Locate platelets.
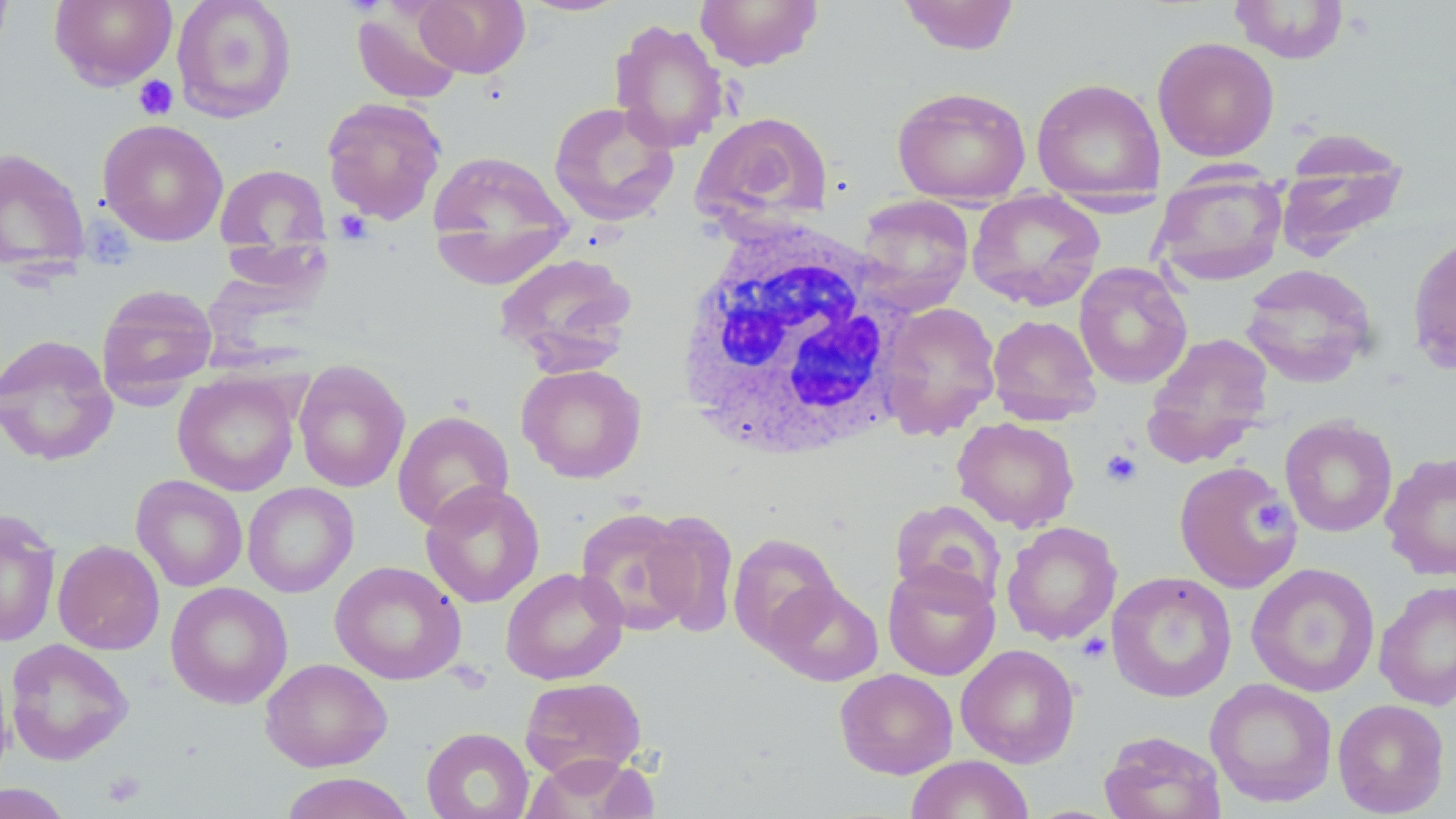
Approximate bounding boxes as (x1, y1, x2, y2) in pixels.
Platelets: (133, 75, 178, 120), (335, 210, 373, 242), (1100, 449, 1143, 488), (1250, 497, 1294, 537), (1077, 633, 1112, 663), (101, 769, 145, 808).

Uninfected red blood cell locations: (0, 0, 14, 65), (49, 0, 178, 89), (171, 0, 297, 123), (413, 0, 531, 78), (517, 0, 630, 17), (694, 0, 824, 71), (897, 0, 1020, 55), (1229, 0, 1350, 64), (351, 3, 466, 106), (609, 18, 730, 153), (1152, 36, 1280, 161), (1031, 78, 1165, 199), (891, 86, 1031, 205), (321, 96, 447, 224), (548, 101, 680, 227), (691, 111, 834, 230), (97, 119, 229, 246), (1276, 133, 1408, 260), (0, 147, 90, 276), (426, 148, 574, 284), (215, 164, 330, 254), (1151, 170, 1288, 286), (966, 191, 1106, 312), (855, 195, 975, 313), (1407, 233, 1456, 376), (493, 251, 639, 374), (1073, 262, 1193, 389), (1239, 263, 1379, 389), (96, 283, 218, 404), (879, 302, 1002, 439), (987, 314, 1102, 425), (1143, 332, 1274, 463), (0, 333, 119, 466), (293, 359, 411, 493), (516, 363, 647, 484), (173, 371, 301, 496), (393, 410, 514, 531), (1279, 416, 1398, 537), (952, 417, 1079, 532), (1380, 451, 1456, 581), (1173, 459, 1301, 593), (132, 474, 248, 592), (243, 482, 359, 598), (420, 482, 545, 607), (889, 498, 1006, 609), (0, 507, 62, 648), (574, 507, 697, 635), (642, 510, 740, 638), (1001, 521, 1123, 646), (727, 532, 842, 653), (52, 539, 165, 655), (330, 561, 466, 685), (882, 562, 1000, 680), (1246, 562, 1380, 697), (501, 567, 628, 685), (1106, 571, 1237, 702), (1373, 579, 1456, 710), (765, 580, 884, 686), (165, 581, 292, 709), (4, 638, 134, 765), (956, 644, 1080, 768), (0, 655, 14, 787), (260, 658, 392, 772), (834, 668, 958, 779), (520, 676, 647, 780), (1205, 678, 1338, 807), (1333, 698, 1450, 817), (420, 727, 535, 819), (1099, 731, 1227, 819), (520, 754, 660, 818), (905, 754, 1034, 818), (279, 772, 416, 819), (0, 783, 74, 819). White blood cell locations: (670, 221, 917, 465). Slide-level diagnosis: no evidence of blood parasites. Single field of view. Captured at 1000x magnification. Light microscopy. Image is 1456×819 pixels. May-Grünwald-Giemsa-stained preparation. Thin blood smear.